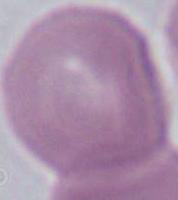
identification: erythrocyte
magnification: 1000x
modality: photomicrograph